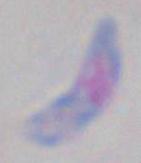

Toxoplasma gondii is shown. Captured at 1000x magnification. Micrograph.